State the preparation type.
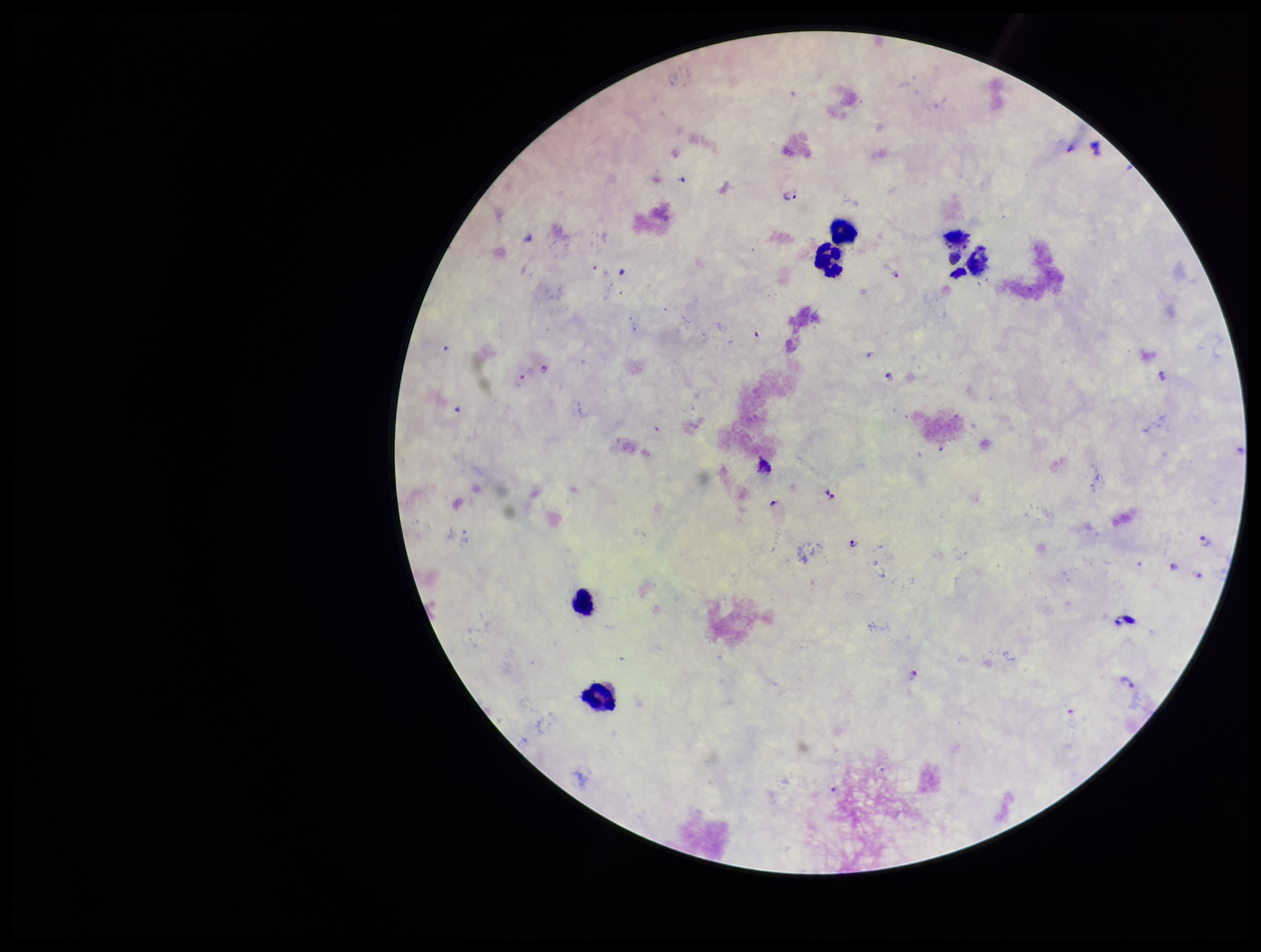

Thick.

Patient malaria status: infected. Stained with Giemsa. Leukocyte count: 5. Species reported for this patient: Plasmodium falciparum. Plasmodium parasites: identified. Parasite count: 13. Single field of view. Smartphone photograph taken through the eyepiece of a microscope. Image is 1261×952 pixels.